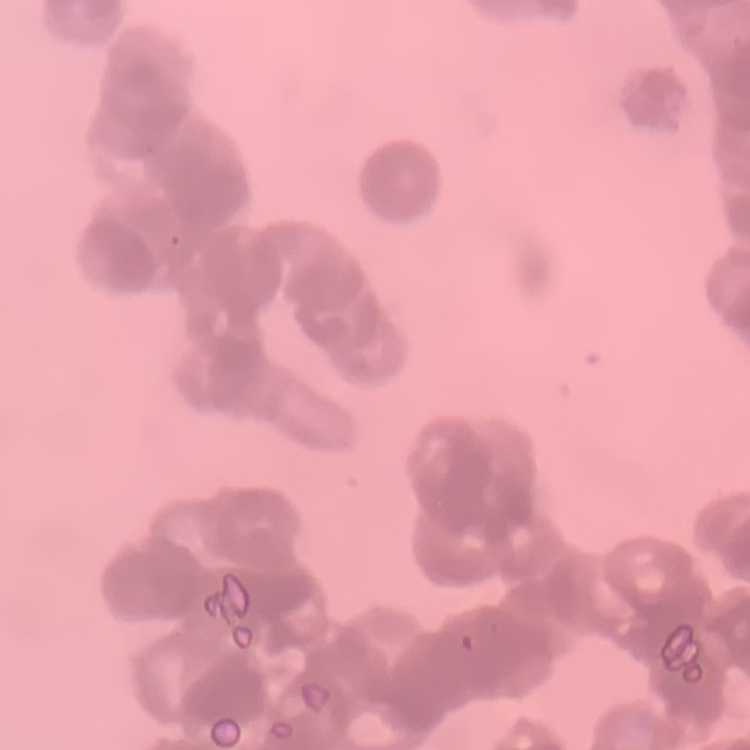

Summary:
  - Red blood cell morphology: rouleaux formation
  - Image type: one tile cut from a larger photomicrograph
  - Preparation: thin peripheral smear
  - Stain: Field's or Giemsa